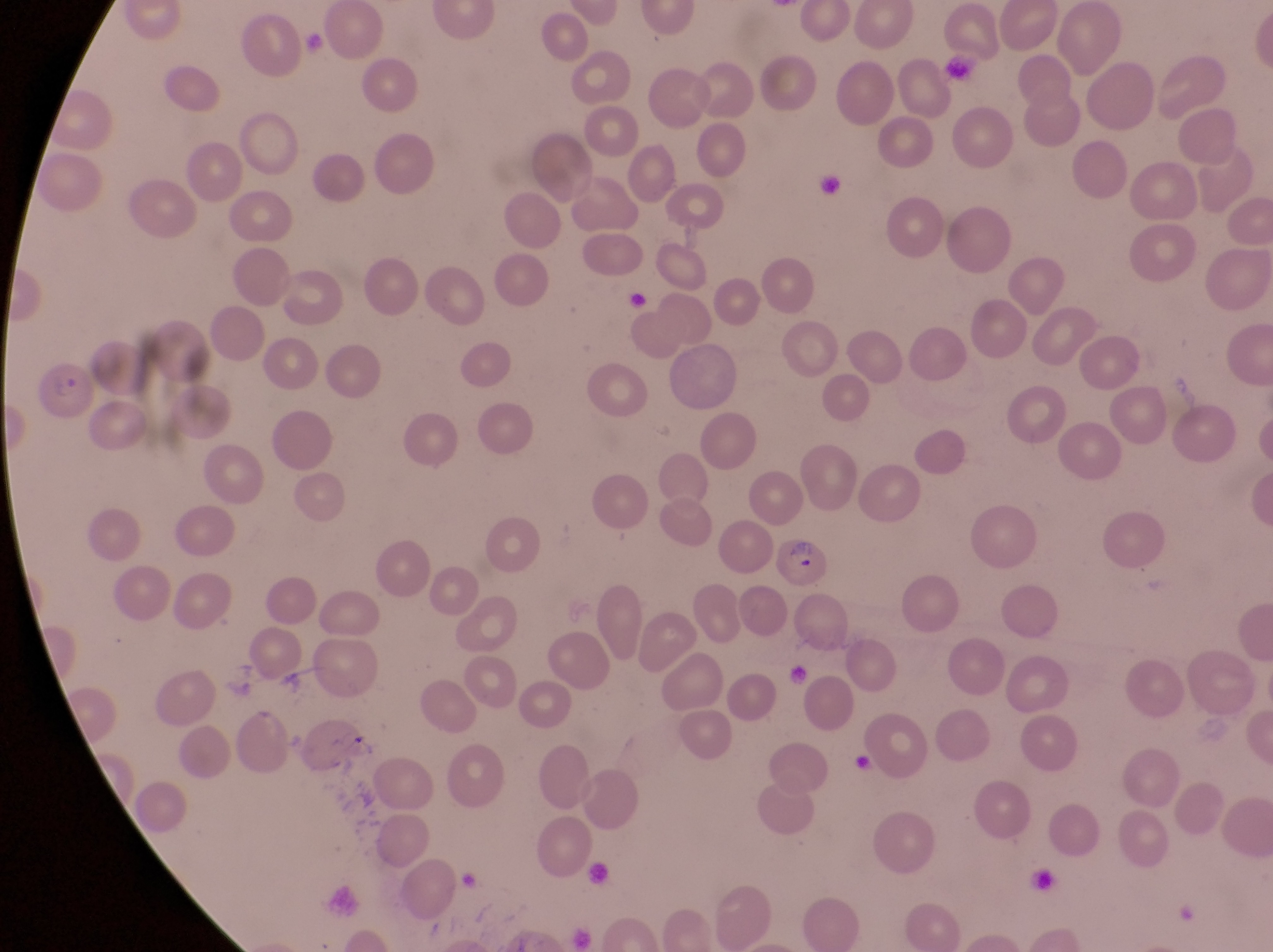 Approximate bounding boxes as (left, top, right, bottom) in pixels. Parasitised red blood cell locations: (30, 362, 97, 429), (771, 532, 838, 594). Trophozoite locations: (847, 744, 879, 783). Artifact (platelet-like body, stain precipitate, or debris) locations: (939, 52, 984, 89), (814, 169, 849, 208), (622, 287, 654, 314), (582, 856, 617, 886), (1026, 867, 1069, 902). Collected in Uganda. Magnification of 1000x. One field of view. Photographed through the eyepiece of an Olympus CX-23 microscope with a smartphone camera. Image is 1273×952 pixels. Thin blood smear.